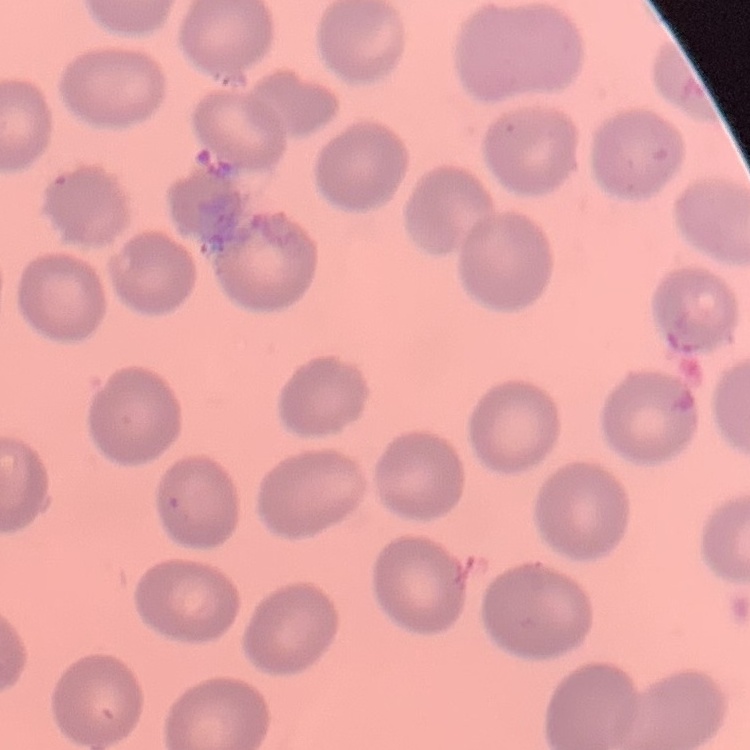

erythrocyte morphology = no rouleaux formation
preparation = thin blood film
stain = Field's or Giemsa
image type = square crop of a larger photomicrograph